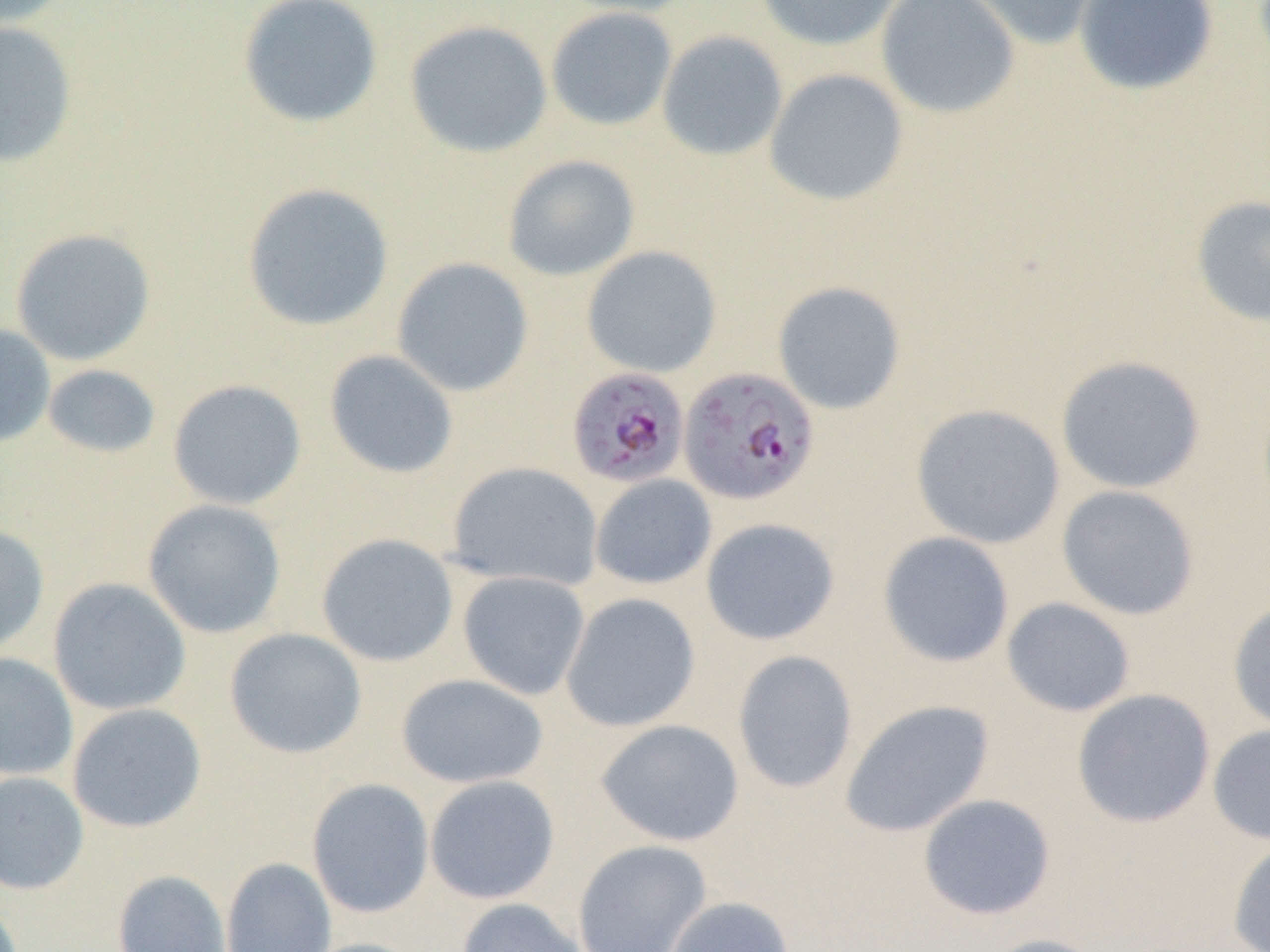
slide-level diagnosis = Plasmodium falciparum
magnification = 1000x
preparation = thin blood smear
image size = 1270×952 pixels
uninfected red blood cell locations = approximate bounding boxes as (x1,y1)-(x2,y2) corner pairs in pixels: (0,0)-(74,29), (238,0)-(383,128), (553,0)-(699,17), (754,0)-(907,52), (876,0)-(1020,119), (956,0)-(1107,51), (1073,0)-(1219,96), (545,7)-(678,131), (0,19)-(79,168), (403,19)-(553,158), (657,30)-(788,161), (764,68)-(909,206), (502,154)-(641,281), (241,182)-(395,332), (1189,194)-(1270,329), (10,227)-(157,366), (581,245)-(722,378), (392,257)-(534,397), (772,280)-(906,414), (0,322)-(56,448), (324,349)-(459,479), (1055,355)-(1207,494), (42,363)-(162,458), (167,379)-(307,510), (910,403)-(1066,549), (446,461)-(603,591), (589,474)-(717,590), (1056,484)-(1200,620), (142,498)-(287,639), (700,517)-(841,646), (0,522)-(50,656), (878,531)-(1015,667), (316,533)-(459,667), (458,571)-(590,700), (48,577)-(192,716), (561,592)-(701,732), (1001,597)-(1136,717), (1227,598)-(1270,735), (224,627)-(367,759), (731,649)-(858,793), (0,652)-(79,781), (396,673)-(549,788), (1072,688)-(1216,828), (840,699)-(995,837), (66,703)-(207,833), (595,718)-(746,847), (1207,723)-(1270,845), (0,770)-(89,895), (424,775)-(561,905), (306,777)-(434,918), (917,793)-(1056,920), (1227,836)-(1270,952), (571,839)-(712,952), (220,856)-(337,952), (112,869)-(232,952), (664,895)-(795,952), (455,897)-(588,952), (980,933)-(1110,952), (295,937)-(430,952)
modality = light microscopy
field of view = one of a larger specimen
Plasmodium falciparum-infected red blood cell locations = approximate bounding boxes as (x1,y1)-(x2,y2) corner pairs in pixels: (678,366)-(821,505), (566,367)-(690,488)